Classify this cell by malaria status.
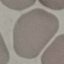
It is uninfected.

capture = smartphone through the microscope eyepiece
preparation = thin blood smear
stain = Giemsa
image type = cell patch, automatically extracted from a larger field of view and resized to 64 × 64 pixels